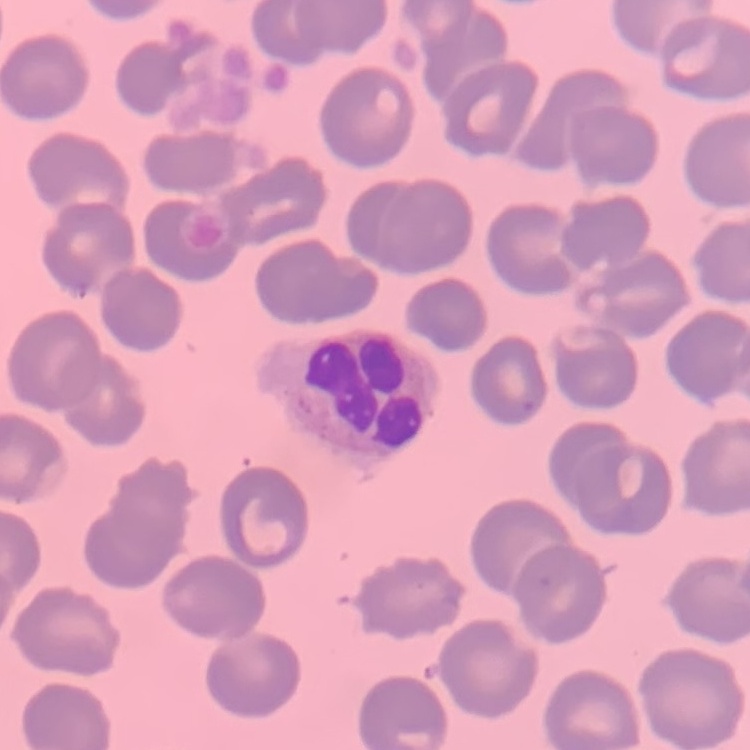
Summary:
  - Erythrocyte morphology: no rouleaux formation
  - Preparation: thin peripheral smear
  - Stain: Field's or Giemsa
  - Image type: square crop of a larger photomicrograph